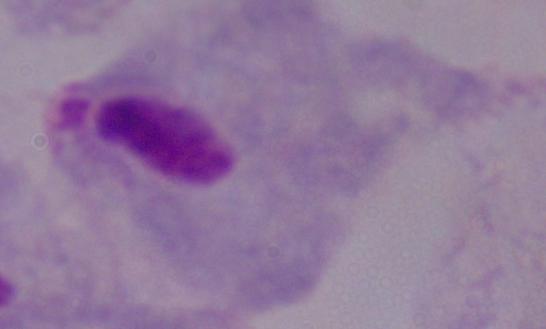

Summary:
  - Identification: trichomonad
  - Modality: photomicrograph
  - Magnification: 1000x